Report the malaria status of this cell.
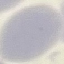
Uninfected.

preparation = thin smear
capture = smartphone through the microscope eyepiece
stain = Giemsa
image type = cell patch, automatically extracted from a larger field of view and resized to 64 × 64 pixels